Point out every malaria parasite and every leukocyte.
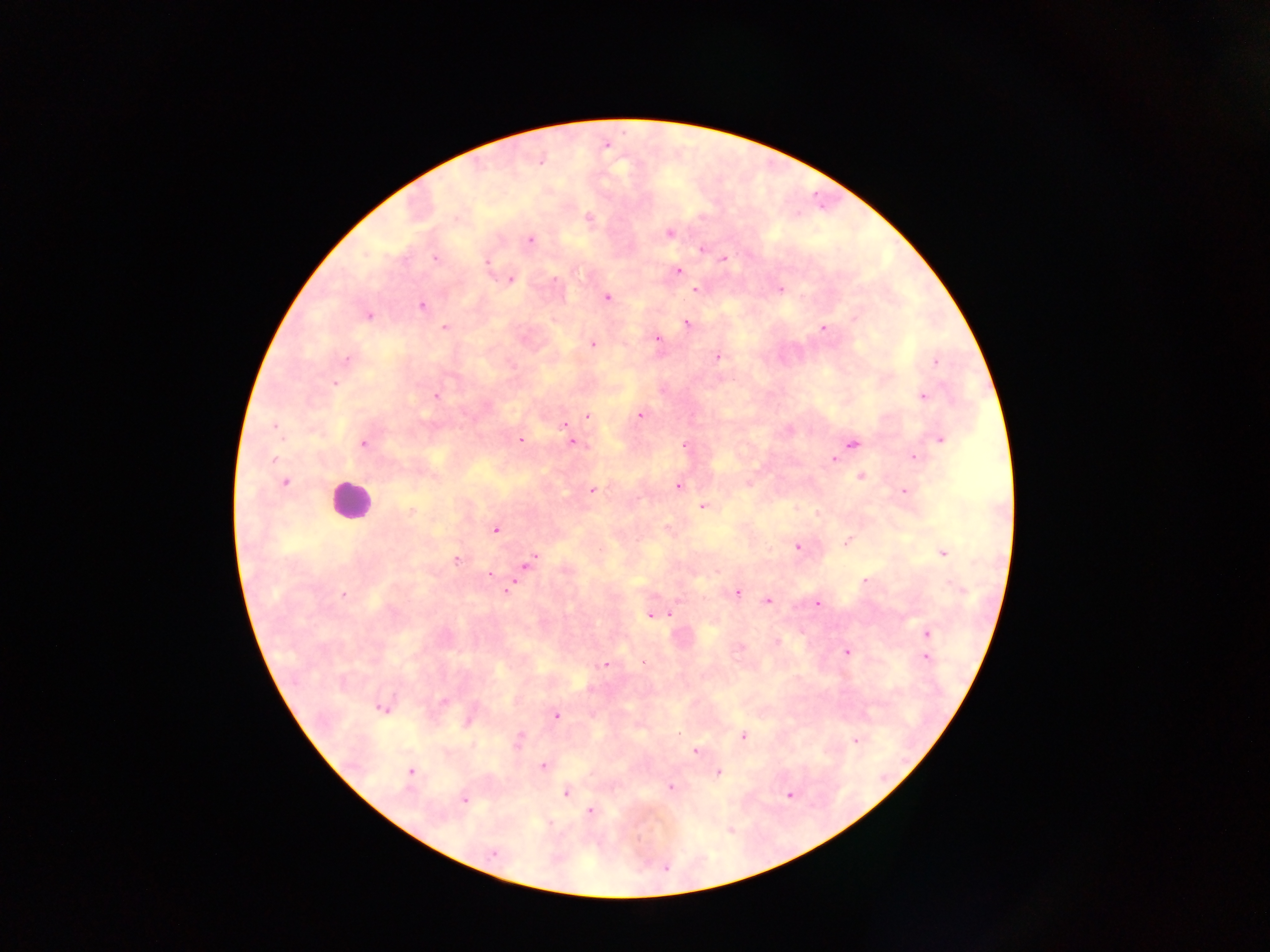

Approximate centers as (x, y) in pixels.
Malaria parasites: (589, 217), (669, 234), (530, 239), (702, 248), (435, 258), (724, 259), (487, 262), (678, 271), (510, 279), (554, 280), (696, 290), (780, 290), (607, 297), (421, 306), (368, 316), (854, 319), (687, 323), (445, 327), (823, 328), (657, 339), (592, 344), (717, 357), (348, 358), (935, 361), (335, 383), (436, 396), (923, 397), (640, 415), (588, 416), (564, 426), (275, 427), (940, 439), (520, 440), (574, 443), (364, 444), (853, 444), (684, 445), (913, 458), (273, 459), (834, 460), (860, 476), (285, 483), (677, 485), (592, 491), (904, 491), (702, 507), (410, 511), (667, 528), (495, 530), (847, 541), (797, 547), (942, 553), (456, 560), (529, 563), (489, 574), (865, 581), (507, 591), (736, 593), (343, 594), (768, 601), (817, 604), (670, 614), (650, 616), (927, 633), (776, 642), (740, 648), (847, 651), (927, 657), (643, 662), (605, 665), (444, 701), (382, 708), (556, 716), (468, 722), (743, 736), (519, 740), (856, 740), (695, 752), (544, 767), (411, 771), (718, 773), (670, 786), (565, 792), (790, 795), (464, 800), (591, 811), (494, 853).
Leukocytes: (349, 500).

Summary:
  - Preparation: thick blood film
  - Country: Ghana
  - Field of view: single
  - Image size: 1270×952 pixels
  - Capture: mobile-phone photograph through a microscope